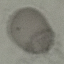
Malaria status: uninfected. Thin blood film. Photographed with a smartphone camera at the microscope eyepiece. Automatically extracted cell patch, resized to 64 × 64 pixels. Giemsa stain.